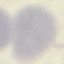
result = negative for malaria parasites
image type = automatically extracted cell patch, resized to 64 × 64 pixels
preparation = thin blood smear
stain = Giemsa
capture = smartphone through the microscope eyepiece